Comment on the morphology of the erythrocytes.
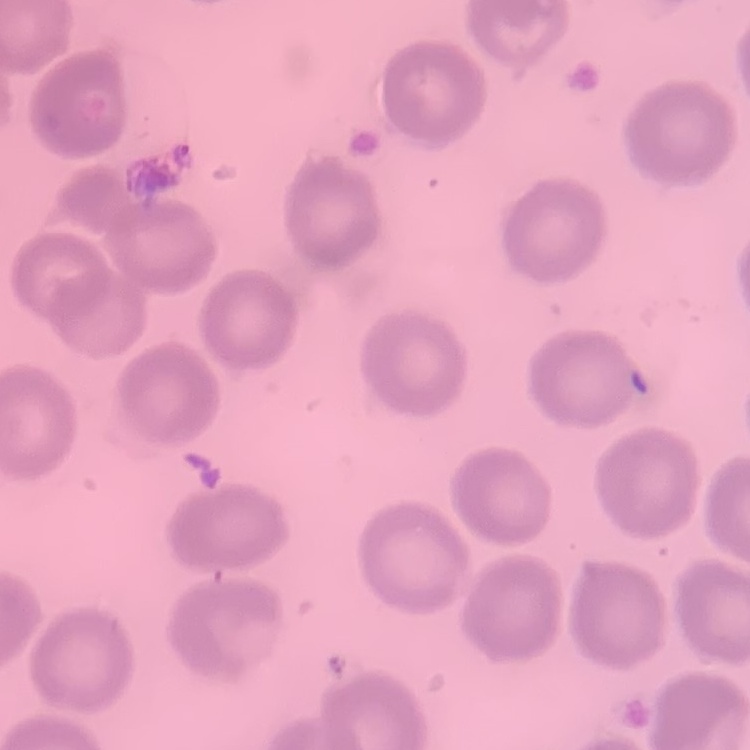

They show no rouleaux formation.

Thin blood film. One tile cut from a larger photomicrograph. Field's or Giemsa stain.